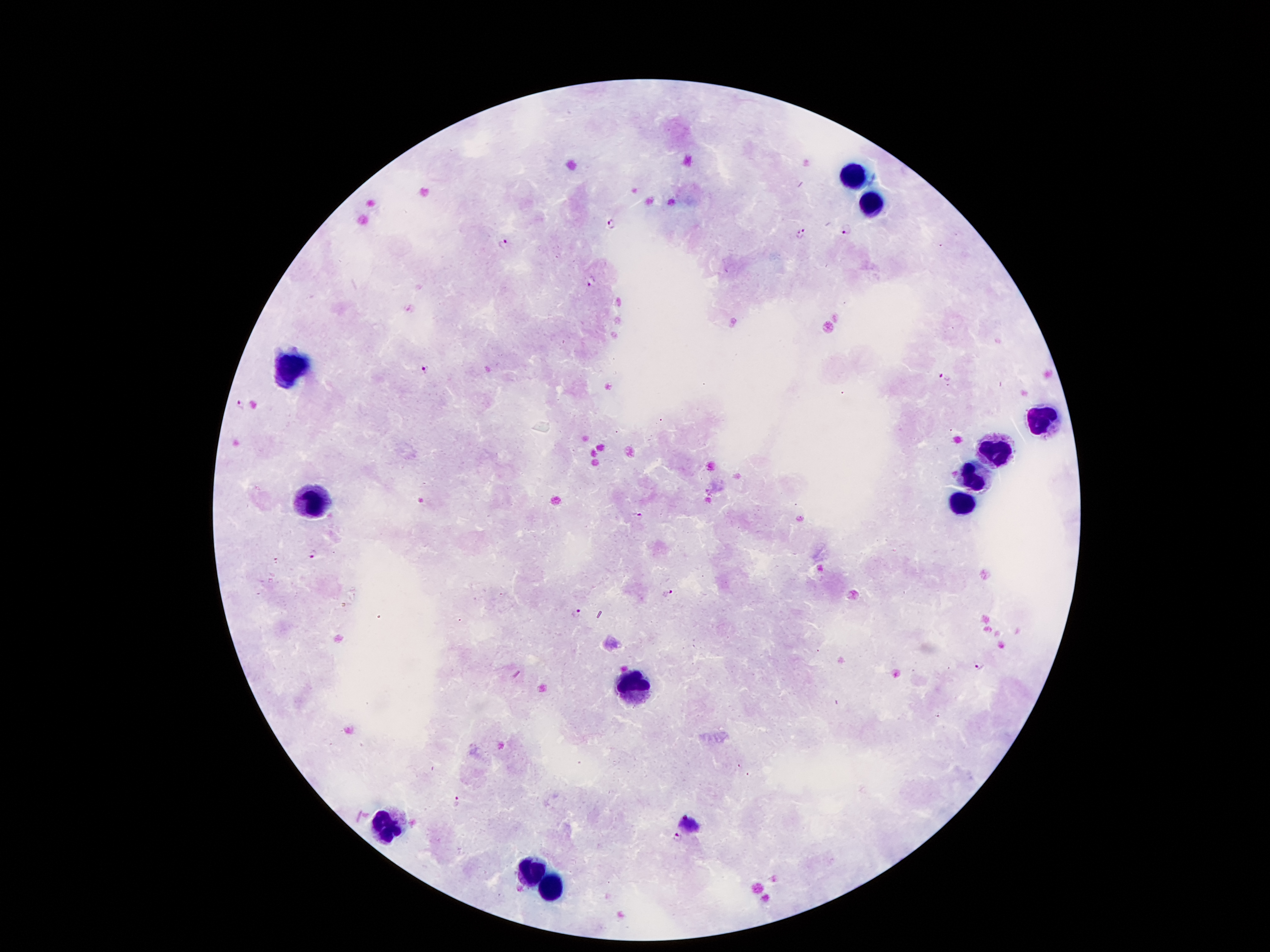

Approximate centers as [x, y] in pixels.
Summary:
  - Plasmodium parasite locations: [612, 225], [846, 230], [801, 235], [504, 244], [589, 281], [425, 369], [944, 378], [240, 406], [639, 516], [314, 555], [667, 591], [576, 614], [979, 665], [455, 803], [691, 822], [678, 839]
  - Leukocyte locations: [852, 176], [870, 205], [288, 367], [1046, 420], [991, 451], [970, 480], [311, 500], [960, 504], [636, 681], [387, 826], [532, 873], [553, 886]
  - Capture: smartphone through the microscope eyepiece
  - Image size: 1270×952 pixels
  - Patient malaria status: positive for Plasmodium falciparum
  - Preparation: thick blood smear
  - Stain: Giemsa
  - Field of view: one from this slide
  - Magnification: 100x